Outline each blood parasite and name the species.
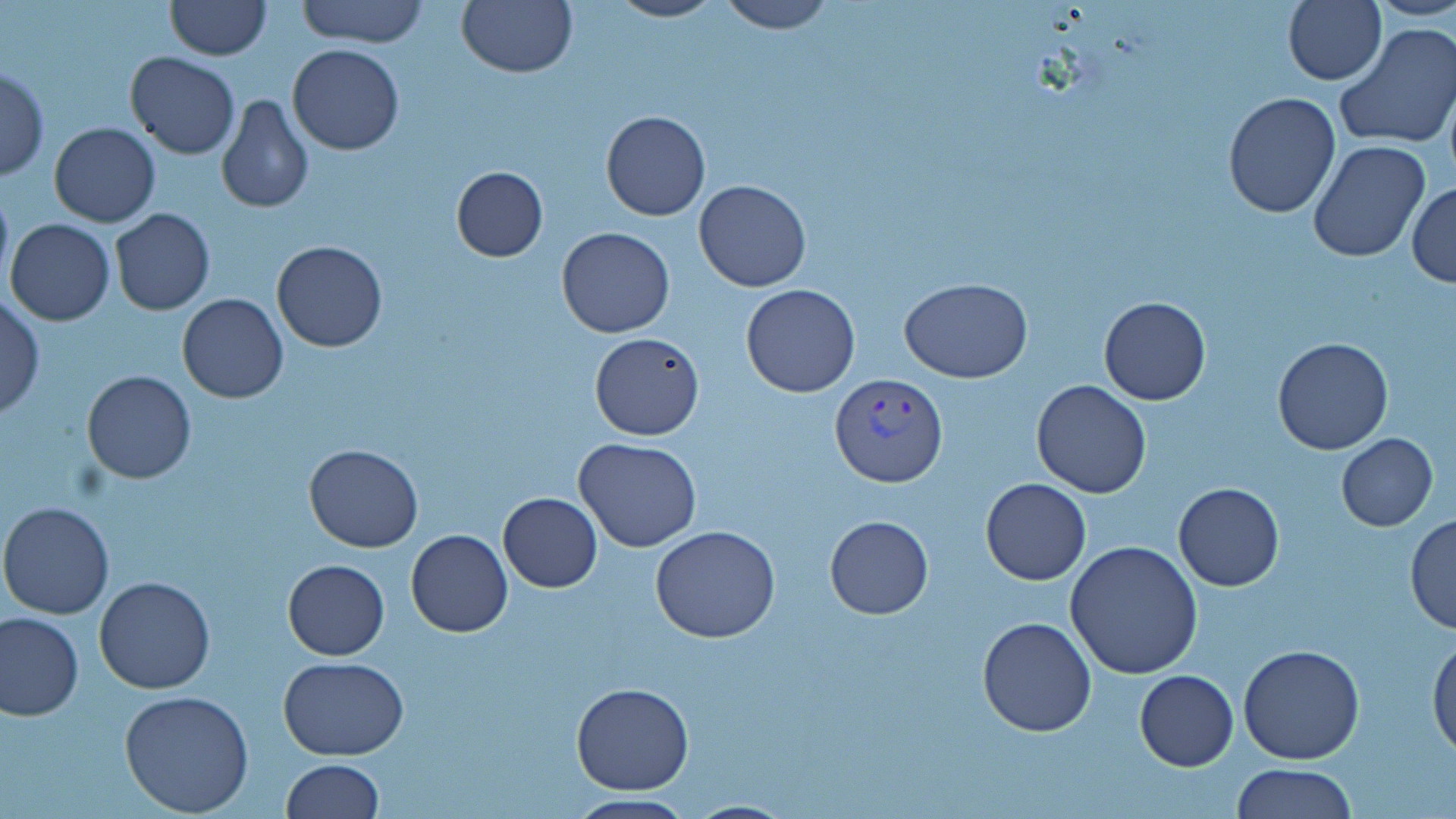

Approximate bounding boxes as [x1, y1, x2, y2] in pixels.
Plasmodium vivax-infected red blood cells: [832, 375, 947, 488].
No Plasmodium falciparum, Plasmodium ovale, Plasmodium malariae, Babesia divergens, or Trypanosoma brucei observed.

slide-level diagnosis = Plasmodium vivax
modality = light microscopy
field of view = one of a larger specimen
image size = 1456×819 pixels
uninfected red blood cell locations = approximate bounding boxes as [x1, y1, x2, y2] in pixels: [166, 0, 270, 59], [298, 0, 428, 48], [456, 0, 578, 79], [605, 0, 727, 23], [713, 0, 837, 34], [1282, 0, 1386, 86], [1373, 0, 1456, 22], [1335, 22, 1456, 154], [287, 43, 404, 156], [125, 52, 239, 160], [0, 67, 49, 181], [216, 93, 314, 214], [1223, 93, 1342, 219], [601, 110, 711, 221], [49, 122, 161, 228], [1307, 139, 1432, 263], [450, 165, 548, 262], [692, 179, 812, 292], [0, 182, 13, 294], [1407, 182, 1455, 288], [109, 210, 215, 315], [5, 218, 114, 325], [555, 226, 675, 337], [272, 241, 388, 352], [901, 278, 1032, 383], [740, 283, 861, 398], [177, 293, 288, 403], [0, 296, 44, 420], [1097, 297, 1212, 405], [590, 333, 706, 440], [1272, 337, 1395, 456], [82, 370, 197, 484], [1030, 380, 1153, 499], [1336, 434, 1438, 532], [574, 437, 703, 553], [302, 443, 424, 551], [981, 478, 1092, 586], [1173, 481, 1285, 591], [498, 492, 603, 593], [1, 500, 117, 619], [1404, 514, 1456, 634], [824, 516, 933, 619], [650, 525, 780, 642], [406, 529, 513, 638], [1064, 540, 1205, 679], [282, 559, 389, 660], [94, 575, 215, 694], [0, 613, 83, 722], [976, 616, 1098, 737], [1429, 634, 1456, 760], [1238, 644, 1365, 765], [280, 655, 408, 759], [1134, 669, 1238, 770], [571, 682, 694, 794], [119, 689, 255, 817], [281, 758, 383, 818], [1230, 763, 1357, 818], [562, 792, 699, 819], [683, 797, 797, 818]
preparation = thin blood smear
stain = May-Grünwald-Giemsa
magnification = 1000x